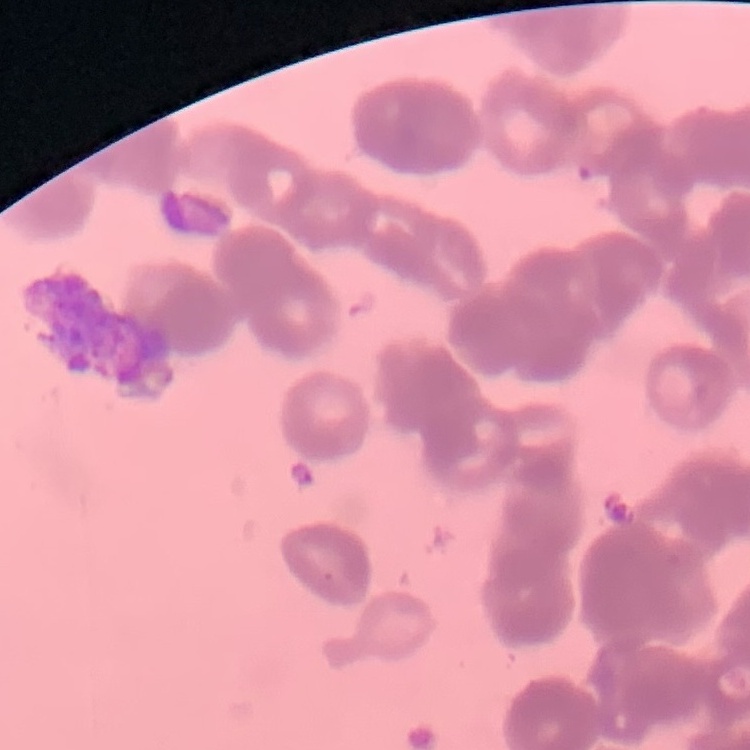

Summary:
  - Red blood cell morphology: rouleaux formation
  - Stain: Field's or Giemsa
  - Image type: one tile cut from a larger photomicrograph
  - Preparation: thin blood smear